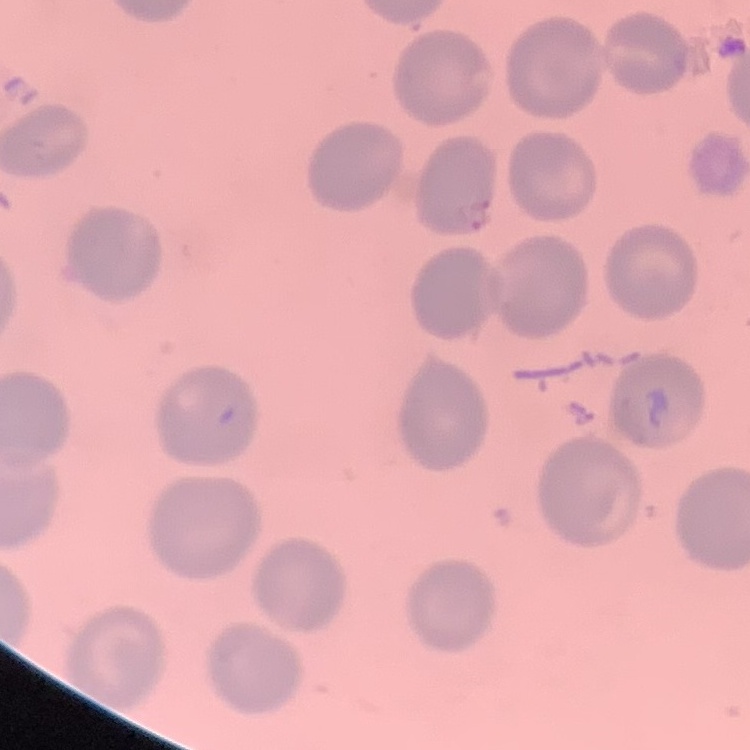
The red blood cells exhibit no rouleaux formation. Square crop of a larger photomicrograph. Thin blood film. Field's or Giemsa stain.